Classify this cell by malaria status.
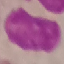

It is uninfected.

Summary:
  - Image type: automatically extracted cell patch, resized to 64 × 64 pixels
  - Stain: Giemsa
  - Capture: smartphone through the microscope eyepiece
  - Preparation: thin blood film